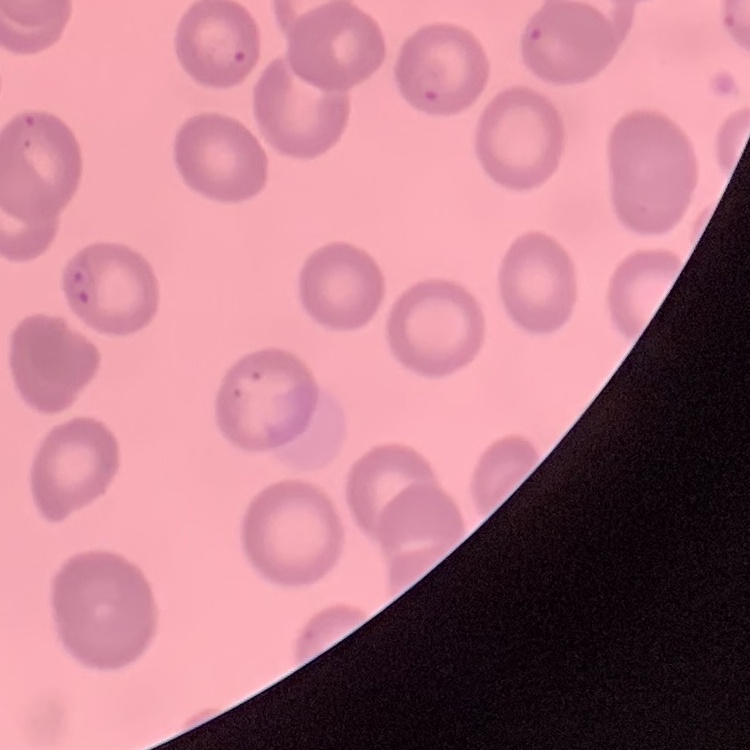 The erythrocytes show no rouleaux formation. One tile cut from a larger photomicrograph. Thin peripheral smear. Field's or Giemsa stain.